Assess this cell for malaria.
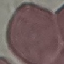

It is uninfected.

Summary:
  - Capture: smartphone through the microscope eyepiece
  - Image type: automatically extracted cell patch, resized to 64 × 64 pixels
  - Preparation: thin blood film
  - Stain: Giemsa